State the preparation type.
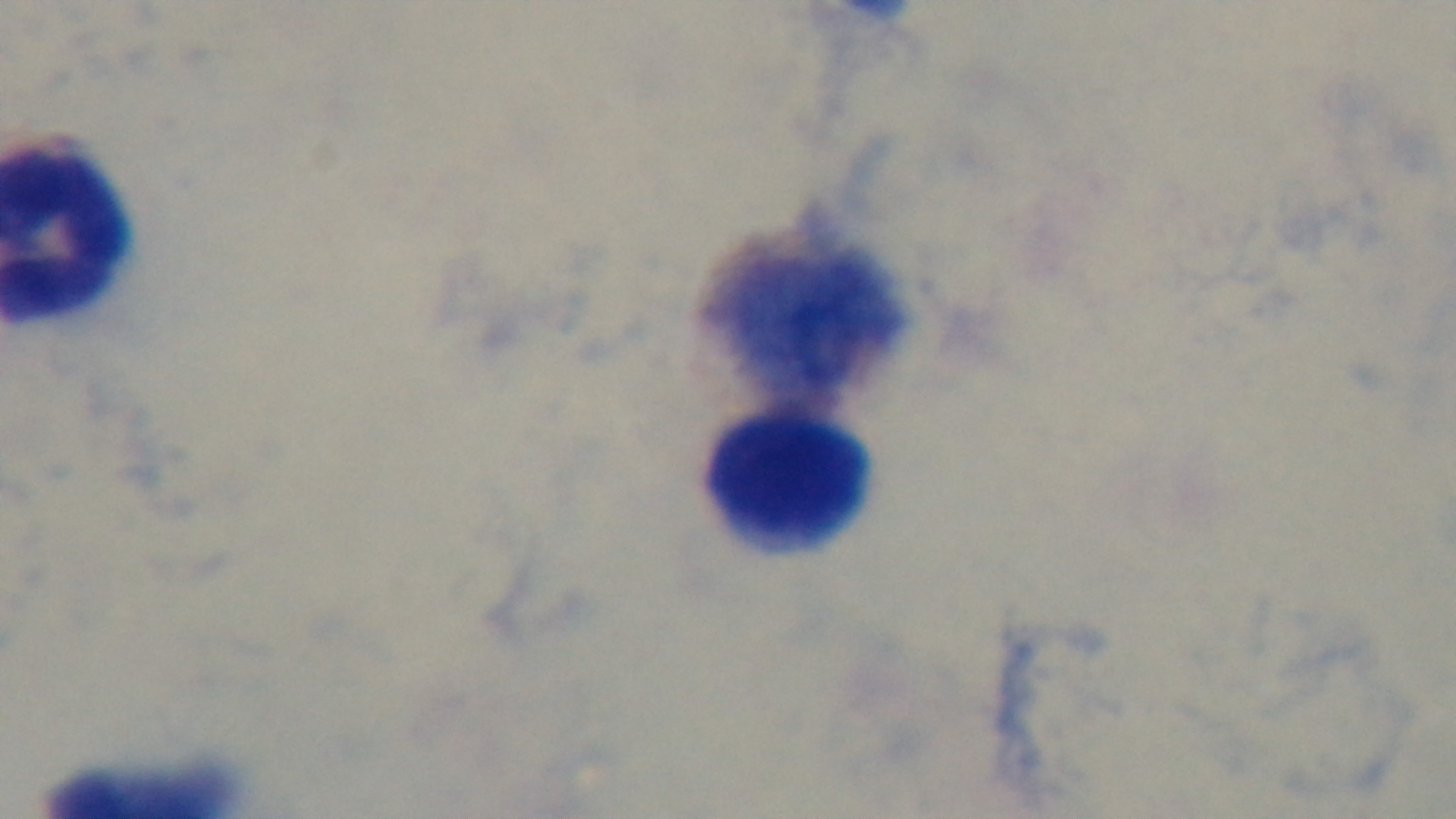
It is a thick blood film.

modality: light microscopy
malaria_status: uninfected
stain: Giemsa
capture: mounted 4K digital camera
objective: 100x oil immersion
field_of_view: one from the slide